Report the malaria status of this cell.
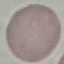
It is uninfected.

Photographed with a smartphone camera at the microscope eyepiece. Thin smear of blood. Giemsa-stained preparation. Cell patch, automatically extracted from a larger field of view and resized to 64 × 64 pixels.